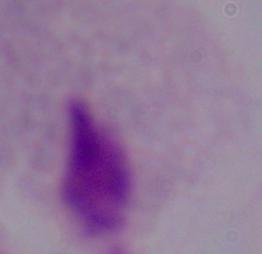

identification = trichomonad
modality = photomicrograph
magnification = 1000x